Assess the morphology of the erythrocytes.
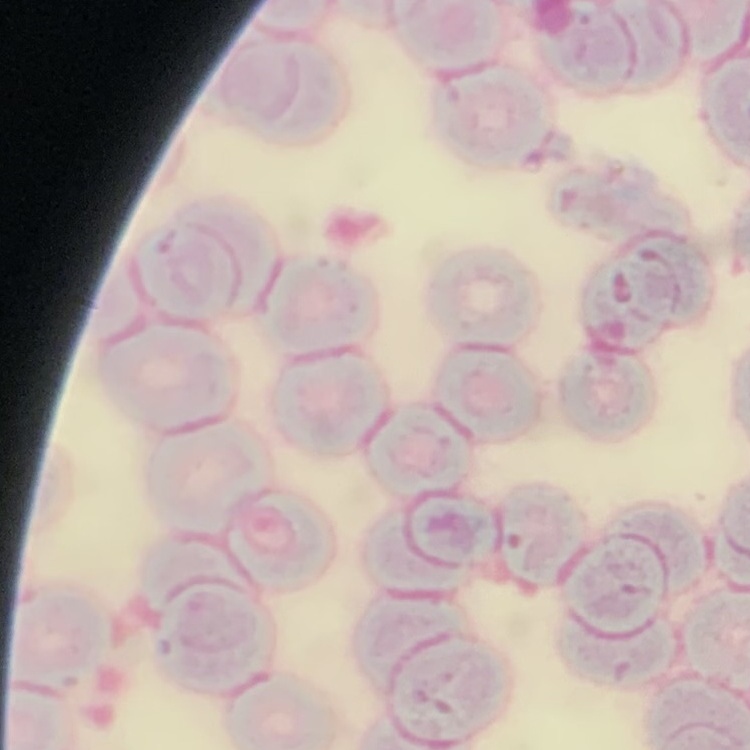

They show rouleaux formation.

preparation = thin blood film
image type = one tile cut from a larger photomicrograph
stain = Field's or Giemsa